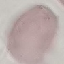 Malaria status: uninfected. Giemsa stain. Cell patch, automatically extracted from a larger field of view and resized to 64 × 64 pixels. Photographed with a smartphone camera at the microscope eyepiece. Thin smear of blood.